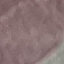 Malaria status: uninfected. Giemsa stain. Automatically extracted cell patch, resized to 64 × 64 pixels. Thin blood film. Acquired by smartphone through the microscope eyepiece.